Give the position of every Plasmodium parasite visible.
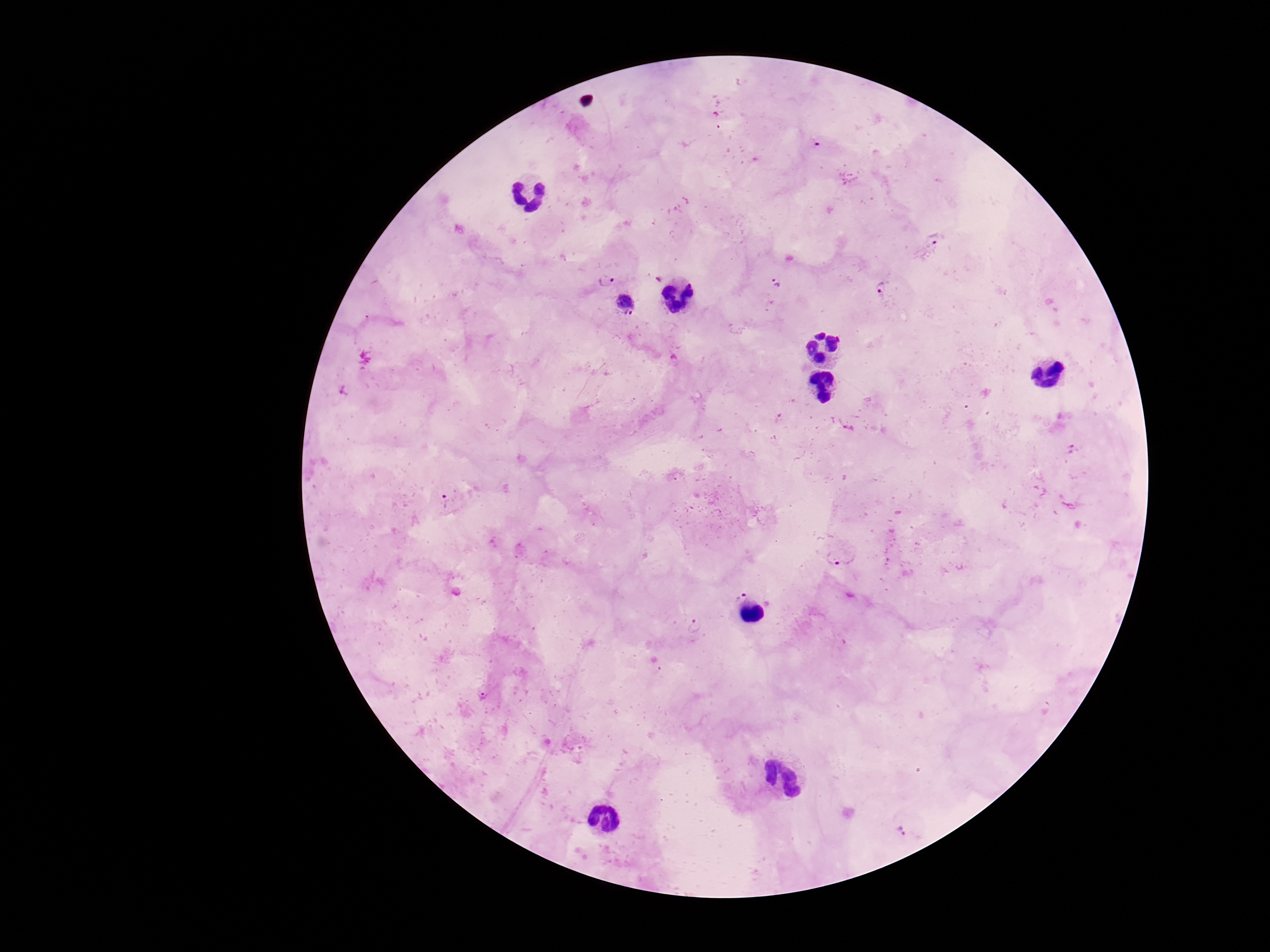
Approximate centers as {x, y} in pixels.
Plasmodium parasites: {937, 240}, {605, 280}, {777, 283}, {883, 287}, {627, 303}, {345, 390}, {1073, 450}, {446, 501}, {833, 557}, {739, 594}, {695, 627}, {901, 829}.

stain: Giemsa
magnification: 100x
preparation: thick blood film
patient_malaria_status: infected
image_size: 1270×952 pixels
field_of_view: single
capture: smartphone camera through the microscope eyepiece